Point out leukocytes.
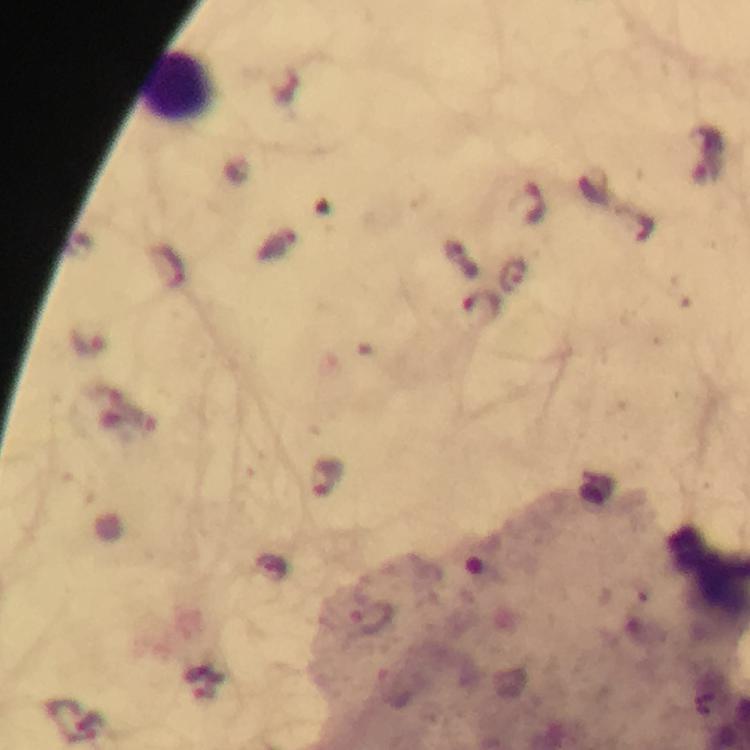
Approximate object centers, in pixels from the top-left corner.
Leukocytes: (x=175, y=87).

Summary:
  - Plasmodium parasite locations: (x=533, y=203), (x=169, y=266), (x=515, y=274), (x=483, y=303), (x=87, y=343), (x=326, y=477)
  - Stain: Giemsa
  - Context: from a diagnostic examination for malaria
  - Immersion oil: applied
  - Magnification: 100x
  - Capture: smartphone camera through the microscope
  - Image size: 750×750 pixels
  - Cropped from: a single field of view
  - Preparation: thick blood smear